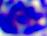

identification = white blood cell
magnification = 400x
modality = micrograph